Report the malaria status of this cell.
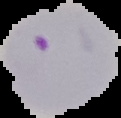
Parasitized.

Summary:
  - Image size: 121×118 pixels
  - Preparation: thin blood smear
  - Image type: segmented cell region on a black background